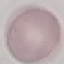
result = no malaria parasites detected
capture = smartphone camera at the microscope eyepiece
image type = cell patch, automatically extracted from a larger field of view and resized to 64 × 64 pixels
stain = Giemsa
preparation = thin smear